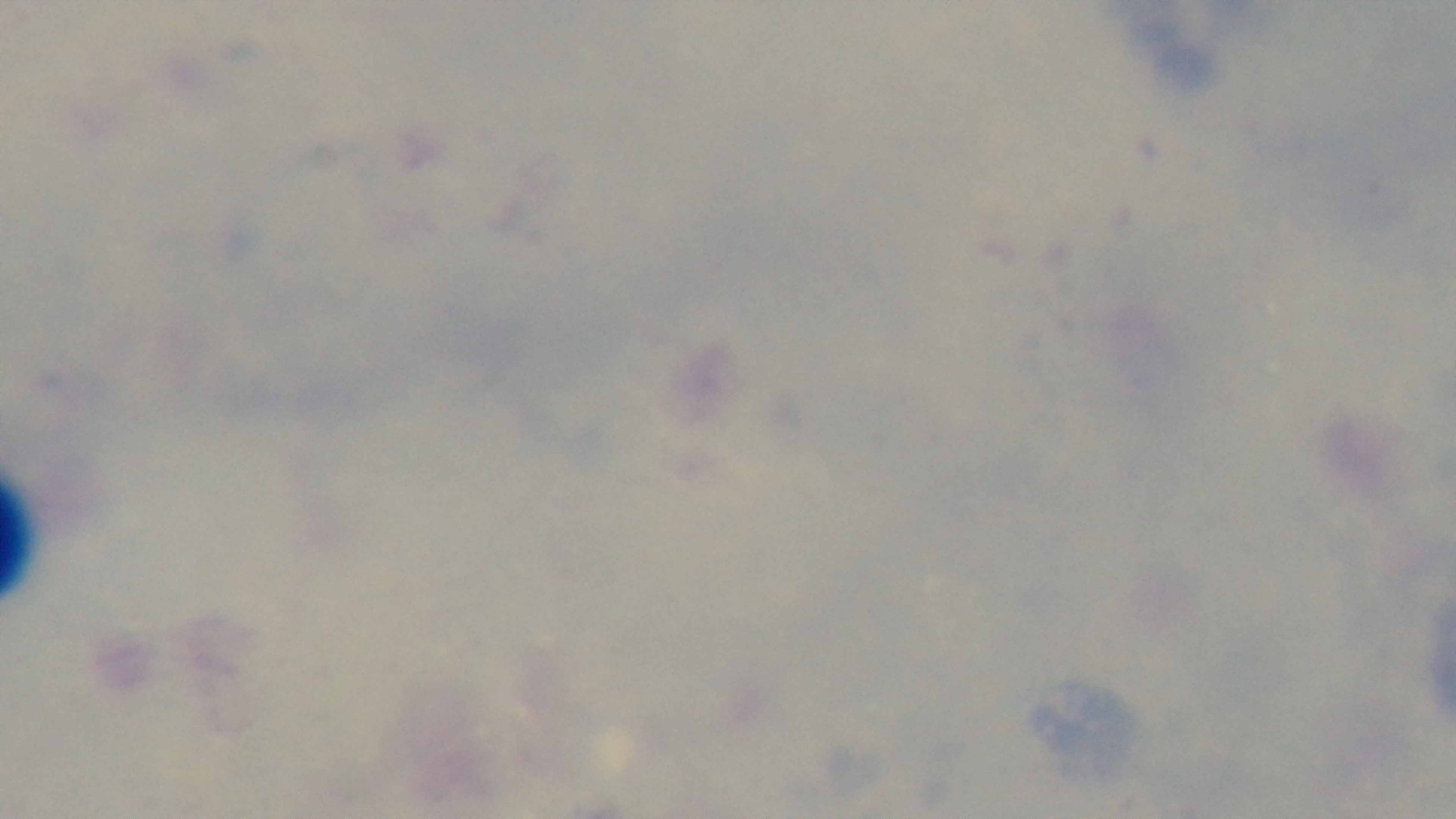
Summary:
  - Field of view: one from the slide
  - Malaria status: uninfected
  - Modality: light microscopy
  - Stain: Giemsa
  - Capture: mounted 4K digital camera
  - Objective: 100x oil immersion
  - Preparation: thick smear